Report the malaria status of this cell.
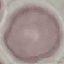
It is uninfected.

stain: Giemsa
capture: smartphone through the microscope eyepiece
preparation: thin smear
image_type: automatically extracted cell patch, resized to 64 × 64 pixels